Look for parasitized red blood cells.
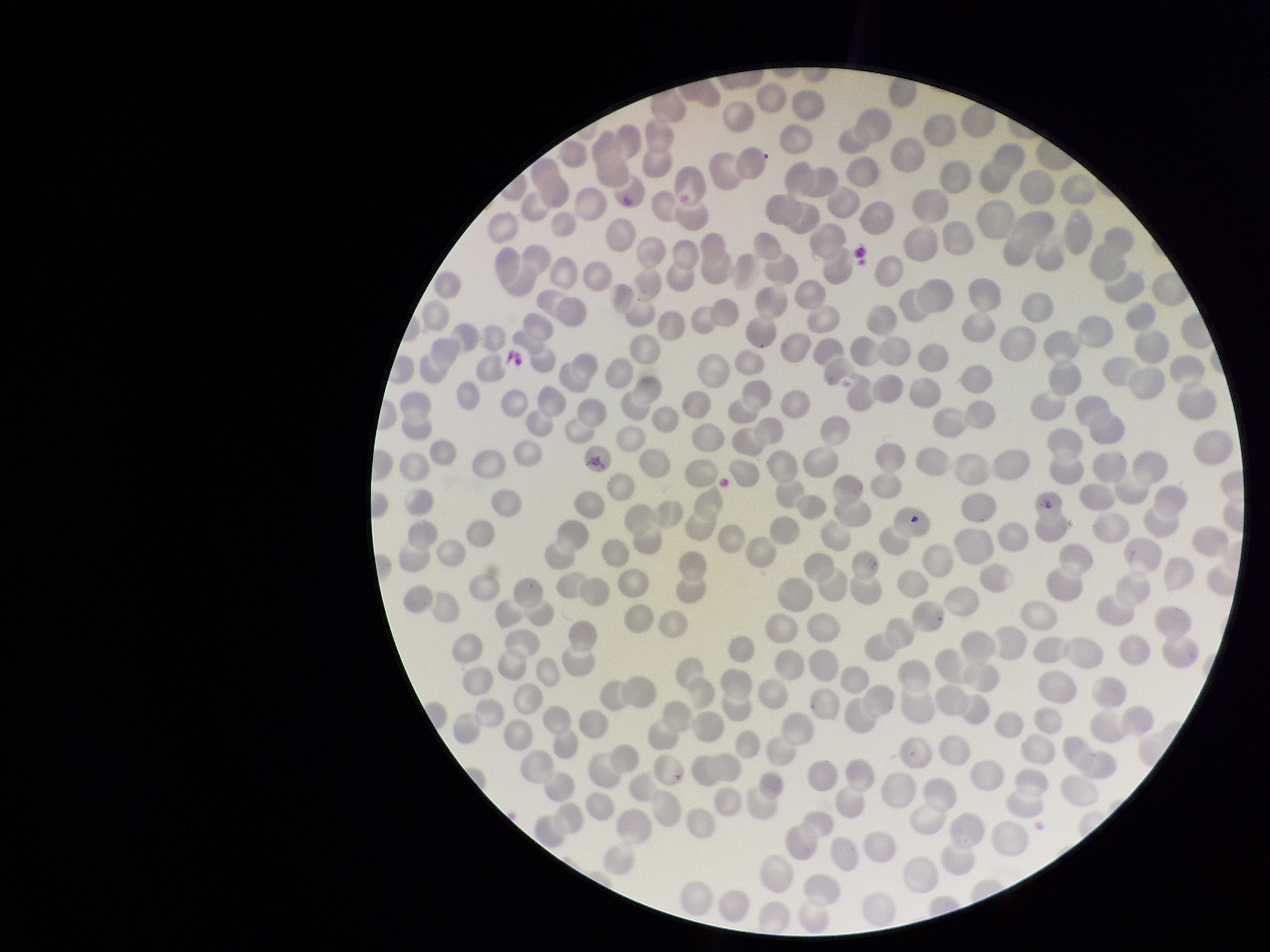
None seen.

Smartphone photograph taken through the eyepiece of a microscope. Parasitized red blood cell count: 0. Patient malaria status: negative. Image is 1270×952 pixels. Preparation: thin blood smear. Giemsa stain. Red blood cell count: 275. One field from this slide.